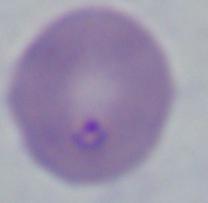

Summary:
  - Magnification: 1000x
  - Modality: micrograph
  - Identification: Babesia